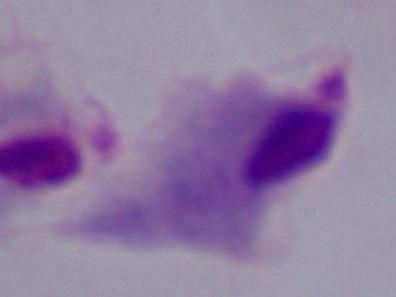

Summary:
  - Modality: photomicrograph
  - Identification: trichomonad
  - Magnification: 1000x